Report the malaria status of this cell.
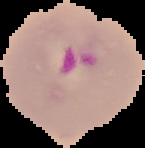
Parasitized.

{
  "image_type": "segmented cell region on a black background",
  "image_size": "145×148 pixels",
  "preparation": "thin blood smear"
}